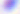
Summary:
  - Identification: Toxoplasma gondii
  - Modality: micrograph
  - Magnification: 400x